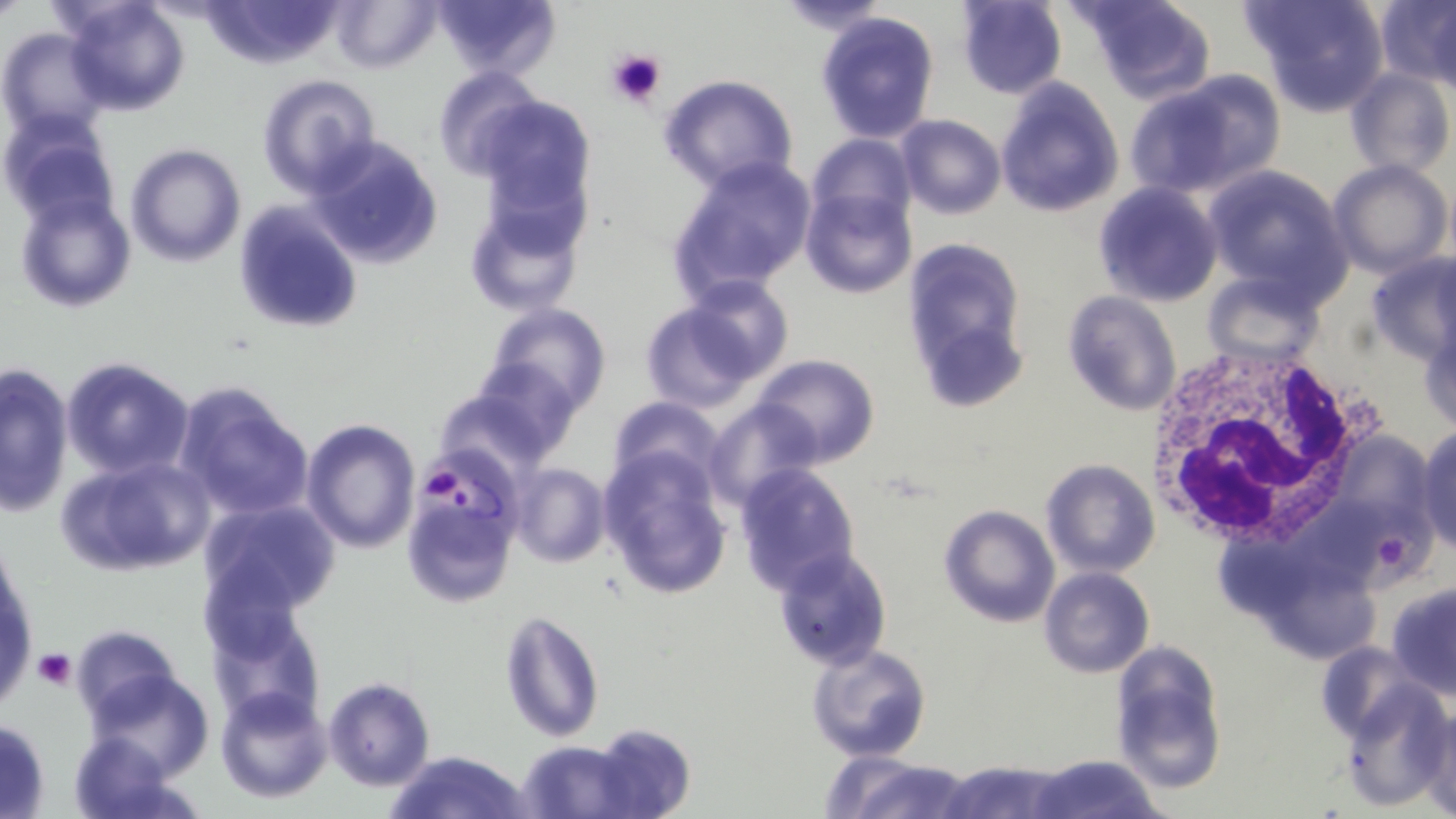

Approximate bounding boxes as (x1, y1, x2, y2) in pixels. Uninfected red blood cell locations: (60, 0, 192, 116), (201, 0, 347, 69), (329, 0, 441, 73), (432, 0, 560, 82), (774, 0, 892, 33), (955, 0, 1067, 98), (1078, 0, 1216, 103), (1243, 0, 1390, 115), (1375, 1, 1456, 87), (1428, 7, 1456, 101), (814, 9, 941, 143), (0, 27, 111, 142), (431, 67, 546, 181), (1343, 68, 1455, 180), (256, 72, 383, 196), (1129, 72, 1285, 199), (657, 73, 800, 194), (994, 75, 1125, 217), (475, 96, 599, 229), (2, 109, 118, 228), (896, 114, 1006, 221), (806, 131, 915, 232), (306, 135, 444, 271), (125, 143, 247, 266), (666, 154, 818, 302), (1328, 159, 1451, 278), (1201, 166, 1353, 305), (1093, 182, 1223, 307), (802, 187, 915, 298), (13, 190, 137, 311), (464, 193, 589, 319), (232, 203, 363, 335), (902, 233, 1031, 411), (1364, 253, 1456, 366), (1202, 270, 1322, 365), (673, 274, 792, 385), (1062, 292, 1181, 416), (638, 300, 763, 412), (482, 302, 613, 418), (1418, 317, 1456, 434), (752, 353, 880, 468), (61, 357, 194, 479), (460, 360, 583, 464), (0, 361, 74, 516), (172, 381, 314, 522), (435, 386, 559, 484), (606, 395, 725, 495), (704, 399, 822, 511), (300, 419, 419, 553), (1414, 427, 1456, 554), (1353, 434, 1434, 530), (598, 445, 732, 598), (59, 453, 214, 578), (1041, 458, 1161, 578), (509, 462, 609, 569), (733, 464, 861, 595), (405, 491, 518, 610), (196, 499, 341, 620), (1323, 500, 1443, 586), (938, 503, 1060, 628), (0, 544, 37, 707), (1213, 545, 1345, 611), (771, 547, 894, 672), (1039, 567, 1155, 678), (1282, 579, 1378, 662), (1387, 580, 1456, 700), (204, 604, 324, 728), (499, 610, 605, 743), (71, 625, 183, 728), (1109, 640, 1228, 794), (1314, 640, 1420, 743), (805, 642, 932, 764), (82, 667, 215, 780), (322, 677, 435, 789), (1339, 681, 1453, 810), (215, 685, 334, 803), (1418, 708, 1456, 817), (0, 717, 51, 817), (590, 724, 695, 818), (66, 729, 192, 819), (517, 739, 632, 818), (385, 749, 532, 819), (1027, 754, 1169, 819), (835, 758, 980, 819), (939, 759, 1066, 819). White blood cell locations: (1142, 345, 1377, 549). Plasmodium falciparum-infected red blood cell locations: (413, 451, 525, 562). Platelet locations: (607, 46, 668, 108), (427, 472, 460, 495), (1377, 541, 1408, 570), (34, 649, 77, 691). Slide-level diagnosis: Plasmodium falciparum. Optical microscopy. Thin blood smear. One field of a larger specimen. Image is 1456×819 pixels. May-Grünwald-Giemsa-stained preparation. 1000x magnification.